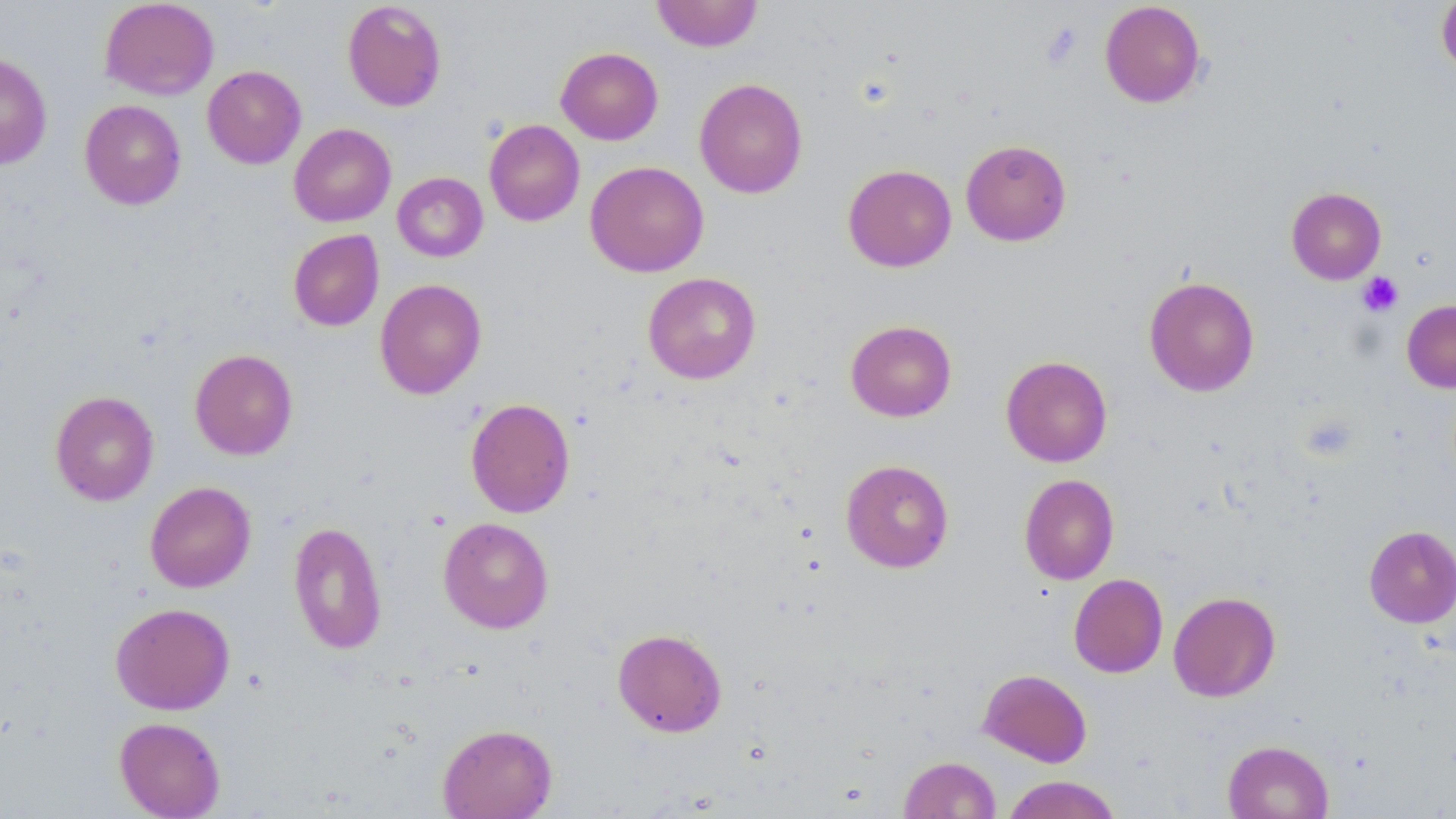 Approximate bounding boxes as [x1, y1, x2, y2] in pixels. Uninfected red blood cell locations: [99, 0, 219, 100], [651, 0, 763, 52], [1436, 0, 1456, 78], [342, 1, 447, 112], [1099, 1, 1207, 108], [555, 46, 663, 145], [0, 52, 52, 169], [202, 65, 306, 169], [694, 78, 808, 198], [79, 99, 186, 209], [484, 120, 585, 227], [289, 123, 396, 227], [960, 139, 1072, 246], [585, 161, 709, 277], [843, 164, 956, 272], [392, 172, 488, 262], [1286, 187, 1386, 284], [288, 229, 384, 332], [643, 272, 761, 384], [1144, 276, 1260, 396], [374, 278, 487, 399], [1401, 299, 1456, 393], [845, 320, 957, 422], [190, 348, 298, 460], [1001, 355, 1113, 467], [50, 390, 159, 506], [465, 397, 575, 518], [841, 459, 954, 573], [1019, 474, 1119, 585], [145, 481, 256, 593], [438, 517, 553, 633], [288, 520, 387, 655], [1364, 525, 1456, 628], [1068, 573, 1168, 678], [1168, 591, 1281, 702], [110, 602, 235, 715], [612, 628, 727, 737], [978, 668, 1092, 768], [114, 717, 226, 818], [438, 723, 557, 819], [1222, 740, 1334, 819], [898, 756, 1001, 818], [1002, 775, 1122, 819]. Platelet locations: [1040, 22, 1084, 69], [1357, 271, 1404, 317]. Slide-level diagnosis: no evidence of blood parasites. May-Grünwald-Giemsa stain. Light microscopy. Thin blood smear. One field of a larger specimen. Image is 1456×819 pixels. 1000x magnification.